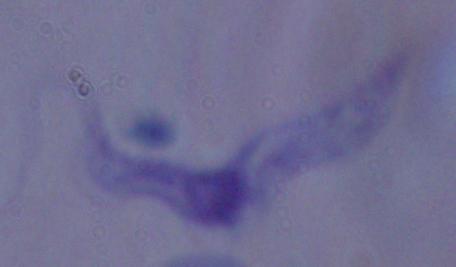 A trypanosome is shown. Micrograph. 1000x magnification.